Locate every blood parasite and identify its species.
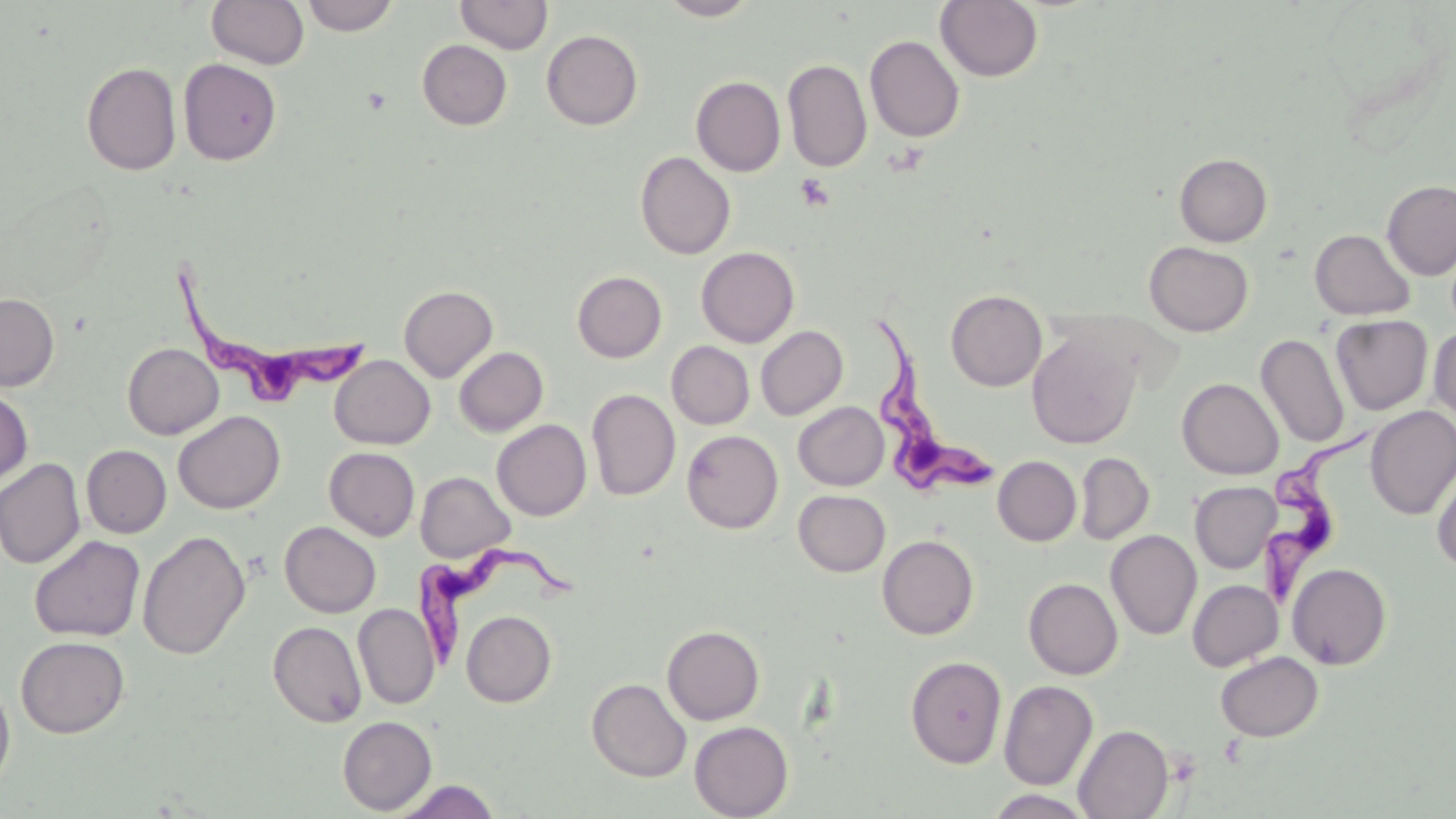

Approximate bounding boxes as [x1, y1, x2, y2] in pixels.
Trypanosoma brucei: [170, 259, 379, 418], [863, 307, 1001, 502], [1259, 432, 1374, 613], [414, 544, 580, 674].
No Plasmodium falciparum, Plasmodium ovale, Plasmodium malariae, Plasmodium vivax, or Babesia divergens observed.

Summary:
  - Platelet locations: [795, 173, 834, 211], [1165, 749, 1202, 786]
  - Uninfected red blood cell locations: [207, 0, 309, 70], [301, 0, 399, 36], [454, 0, 553, 54], [657, 0, 762, 20], [935, 0, 1043, 82], [542, 30, 643, 130], [865, 35, 964, 142], [417, 40, 512, 130], [178, 59, 281, 165], [783, 59, 872, 172], [81, 61, 181, 176], [691, 76, 786, 176], [635, 151, 736, 259], [1175, 153, 1272, 246], [1382, 180, 1456, 279], [1310, 228, 1415, 321], [1144, 241, 1253, 336], [696, 246, 799, 348], [572, 271, 667, 362], [399, 285, 498, 382], [945, 290, 1047, 390], [0, 292, 60, 391], [1330, 315, 1433, 415], [756, 325, 848, 420], [1429, 325, 1456, 425], [1027, 329, 1141, 449], [1256, 333, 1349, 448], [666, 341, 754, 429], [123, 343, 224, 440], [454, 346, 548, 436], [329, 355, 434, 449], [1177, 378, 1284, 479], [0, 388, 33, 487], [586, 388, 680, 501], [793, 401, 888, 490], [1365, 406, 1456, 520], [173, 411, 286, 514], [492, 419, 591, 521], [682, 430, 783, 533], [81, 445, 171, 538], [324, 447, 420, 540], [1075, 452, 1154, 544], [993, 455, 1081, 546], [0, 457, 85, 569], [1431, 458, 1456, 572], [415, 471, 514, 562], [1190, 481, 1281, 573], [793, 490, 890, 576], [279, 521, 380, 617], [1105, 529, 1202, 640], [138, 531, 250, 660], [29, 535, 145, 642], [877, 535, 979, 639], [1287, 562, 1392, 669], [1024, 578, 1122, 679], [1187, 579, 1283, 671], [353, 603, 439, 709], [461, 610, 556, 707], [268, 621, 367, 728], [662, 625, 764, 725], [15, 635, 130, 739], [1215, 651, 1324, 742], [905, 656, 1007, 767], [0, 677, 16, 795], [587, 678, 692, 782], [999, 680, 1097, 790], [337, 716, 437, 815], [689, 721, 793, 819], [1074, 725, 1173, 818], [393, 780, 501, 819], [984, 789, 1096, 818]
  - Slide-level diagnosis: Trypanosoma brucei
  - Modality: optical microscopy
  - Magnification: 1000x
  - Field of view: one of a larger specimen
  - Preparation: thin blood film
  - Stain: May-Grünwald-Giemsa
  - Image size: 1456×819 pixels